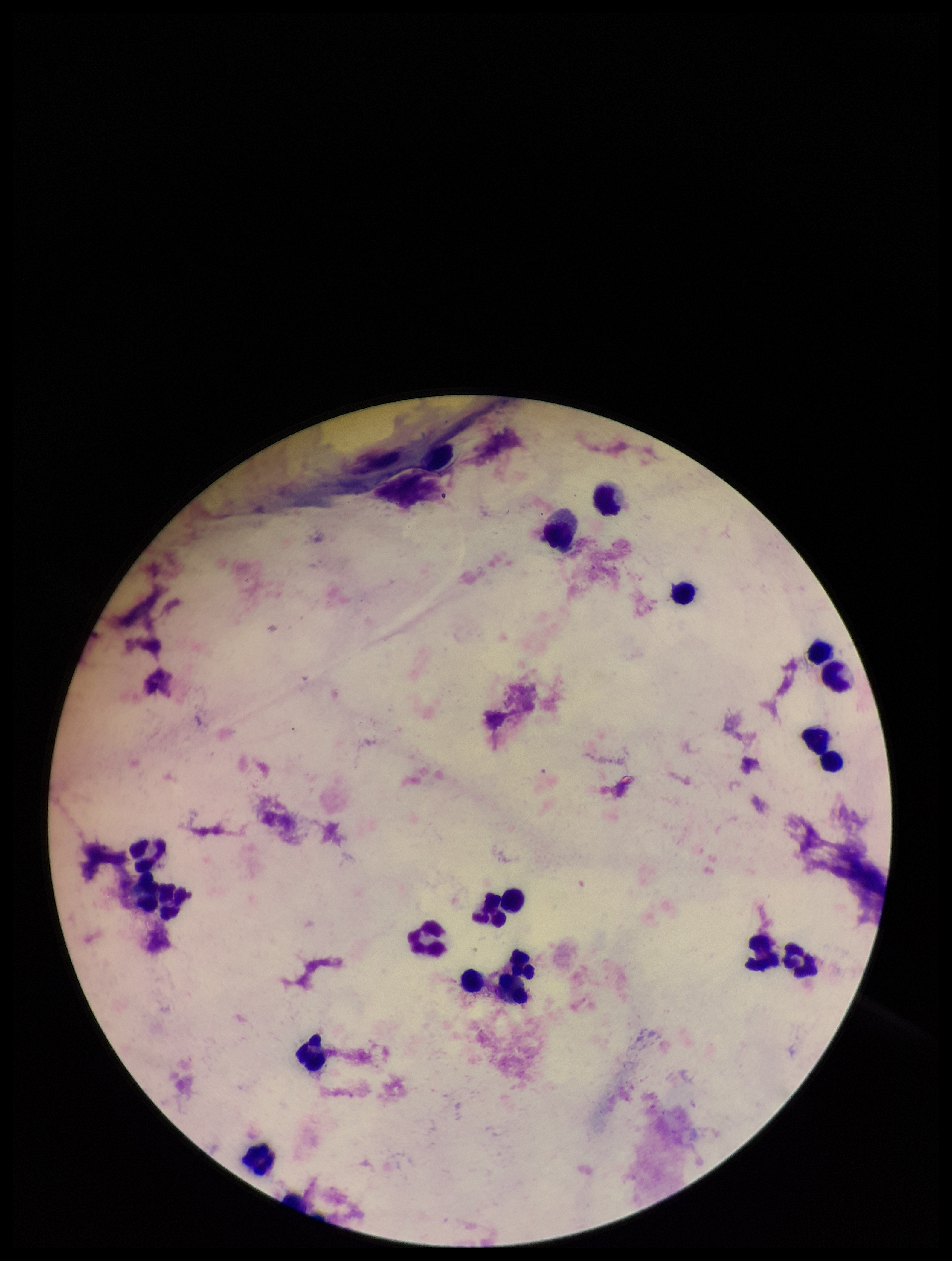

Plasmodium parasites = none seen
field of view = single
preparation = thick
parasite count = 0
leukocyte count = 21
capture = smartphone photograph through the microscope eyepiece
patient malaria status = negative
image size = 952×1261 pixels
stain = Giemsa